Describe the morphology of the red blood cells.
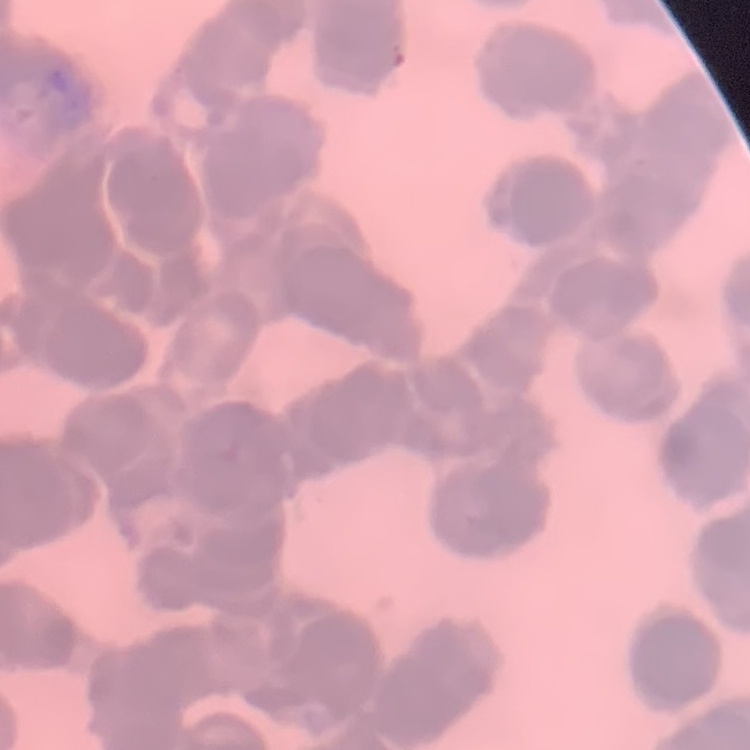

Rouleaux formation.

stain = Field's or Giemsa
preparation = thin blood film
image type = square crop of a larger photomicrograph